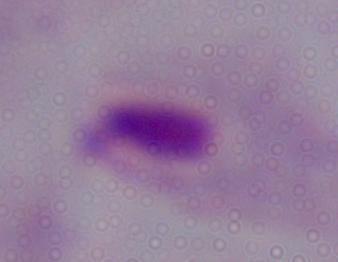
Summary:
  - Modality: photomicrograph
  - Identification: trichomonad
  - Magnification: 1000x